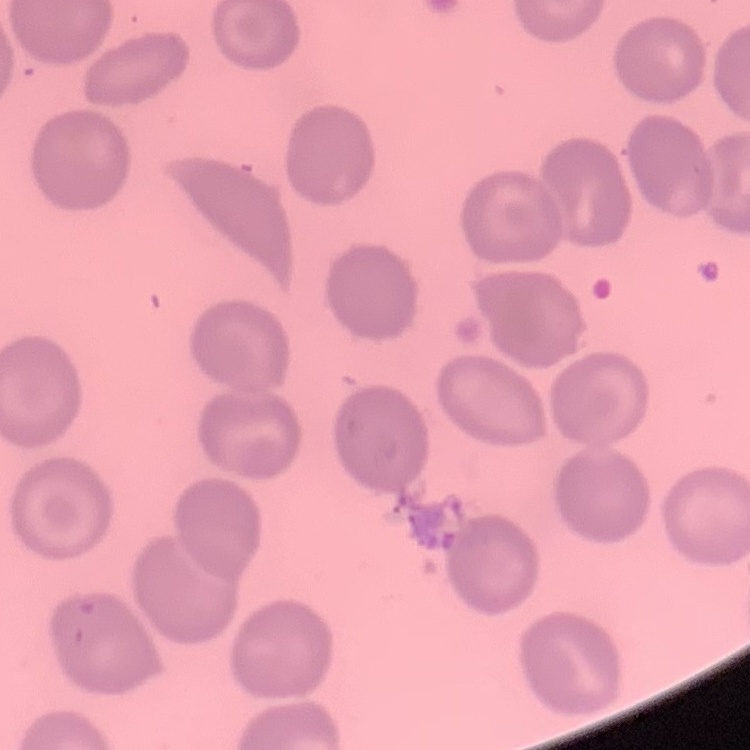
erythrocyte morphology = no rouleaux formation
image type = square crop of a larger photomicrograph
stain = Field's or Giemsa
preparation = thin blood smear